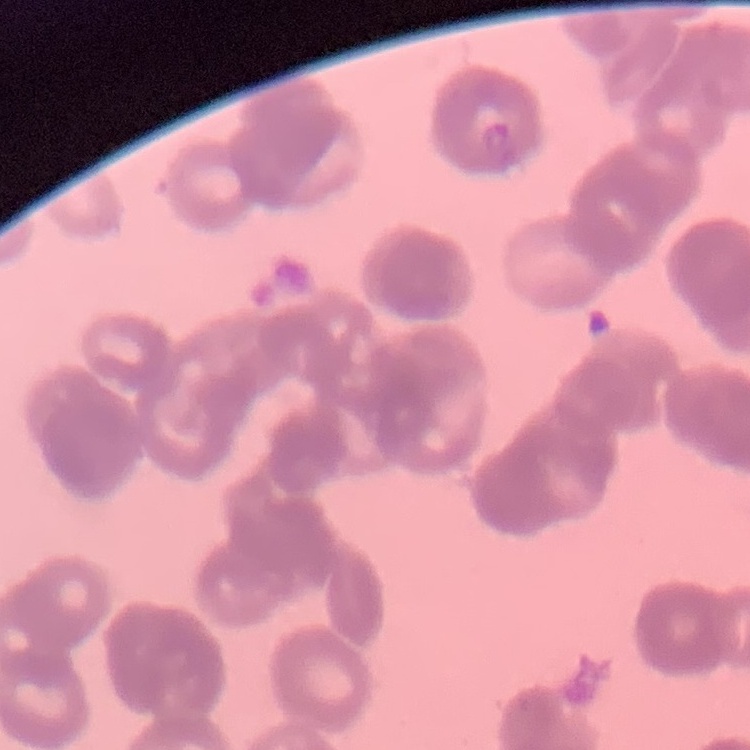

Summary:
  - Red blood cell morphology: rouleaux formation
  - Preparation: thin peripheral smear
  - Image type: square crop of a larger photomicrograph
  - Stain: Field's or Giemsa